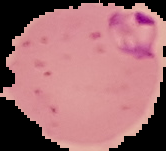
image size = 166×151 pixels
result = Plasmodium parasites identified
preparation = thin blood film
image type = cell region segmented out of the field of view; surrounding area masked to black